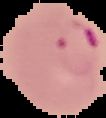

Summary:
  - Image type: segmented cell region on a black background
  - Preparation: thin blood smear
  - Malaria status: parasitized
  - Image size: 106×118 pixels